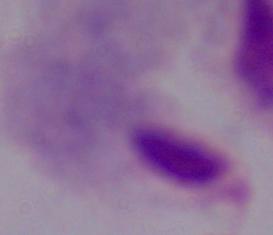
Captured at 1000x magnification. Photomicrograph. A trichomonad is seen.